Assess this cell for malaria.
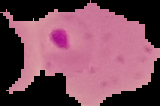

It is parasitized.

preparation: thin blood film
image_type: segmented cell region on a black background
image_size: 160×106 pixels